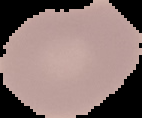

{
  "preparation": "thin blood film",
  "malaria_status": "uninfected",
  "image_type": "cell region segmented out of the field of view; surrounding area masked to black",
  "image_size": "142×118 pixels"
}